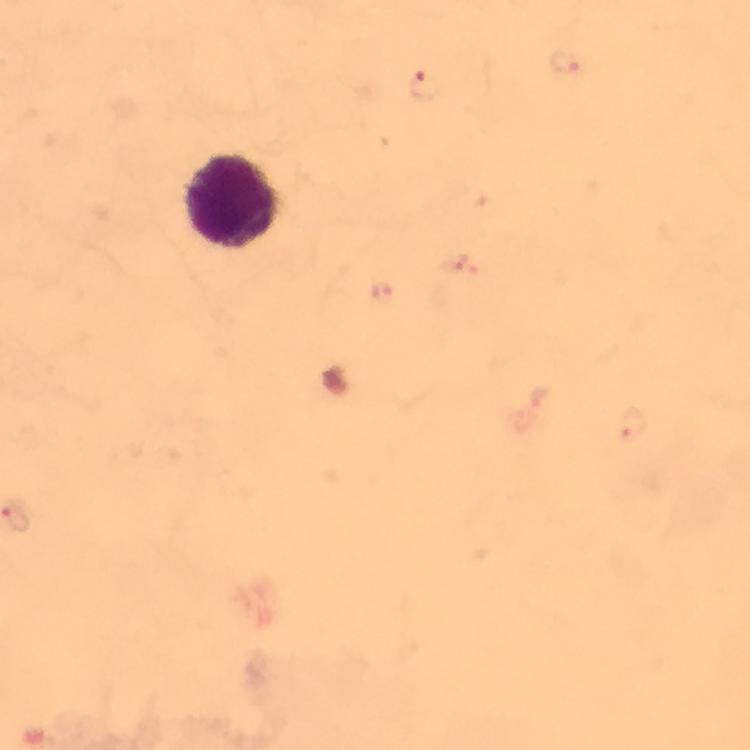
{
  "immersion_oil": "used",
  "malaria_parasite_locations": "approximate centers as [x, y] in pixels: [564, 61], [424, 86], [381, 292], [631, 426]",
  "image_size": "750×750 pixels",
  "leukocyte_locations": "approximate centers as [x, y] in pixels: [238, 205]",
  "stain": "Giemsa",
  "magnification": "100x",
  "context": "from a diagnostic examination for malaria",
  "capture": "smartphone mounted on the microscope",
  "cropped_from": "a single field of view",
  "preparation": "thick blood smear"
}